Assess the morphology of the erythrocytes.
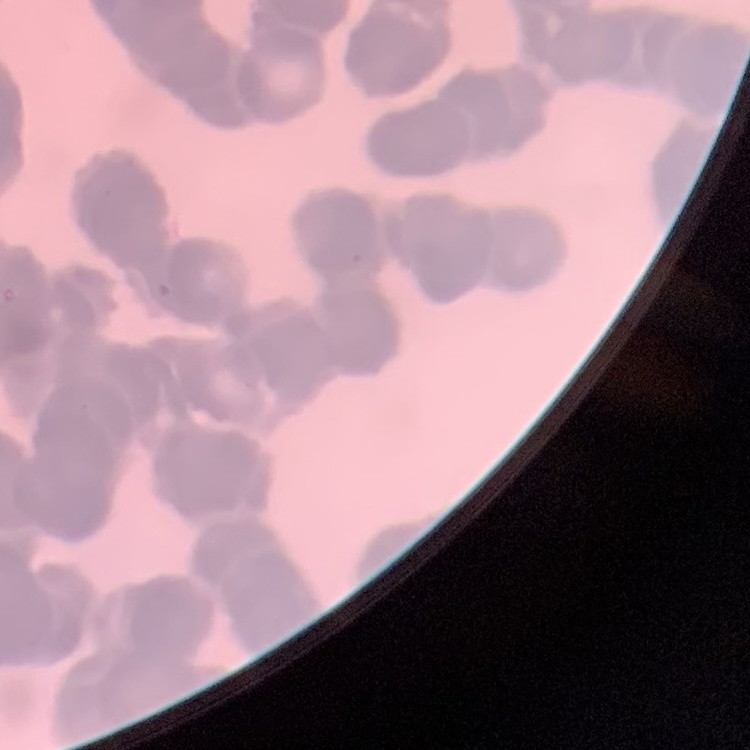
Rouleaux formation.

stain = Field's or Giemsa
preparation = thin blood film
image type = square crop of a larger photomicrograph